Report the malaria status of this cell.
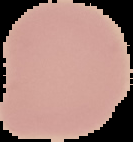

Uninfected.

Image is 133×142 pixels. From a thin blood film. Cell region segmented out of the field of view; the surrounding area is masked to black.